Assess this cell for malaria.
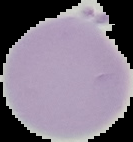

It is uninfected.

preparation = thin blood film
image type = cell region segmented out of the field of view; surrounding area masked to black
image size = 133×142 pixels